Classify this cell by malaria status.
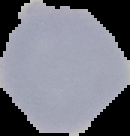

It is uninfected.

From a thin blood film. Image is 130×136 pixels. Segmented cell region on a black background.